Report the malaria status of this cell.
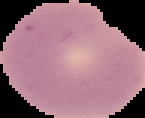

It is uninfected.

Image is 145×118 pixels. From a thin blood film. The area outside the segmented cell region is set to black.